Assess this cell for malaria.
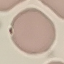
Uninfected.

preparation = thin blood film
capture = smartphone camera at the microscope eyepiece
image type = cell patch, automatically extracted from a larger field of view and resized to 64 × 64 pixels
stain = Giemsa